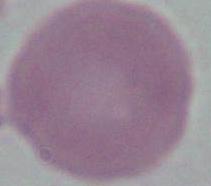

Summary:
  - Modality: photomicrograph
  - Magnification: 1000x
  - Identification: red blood cell